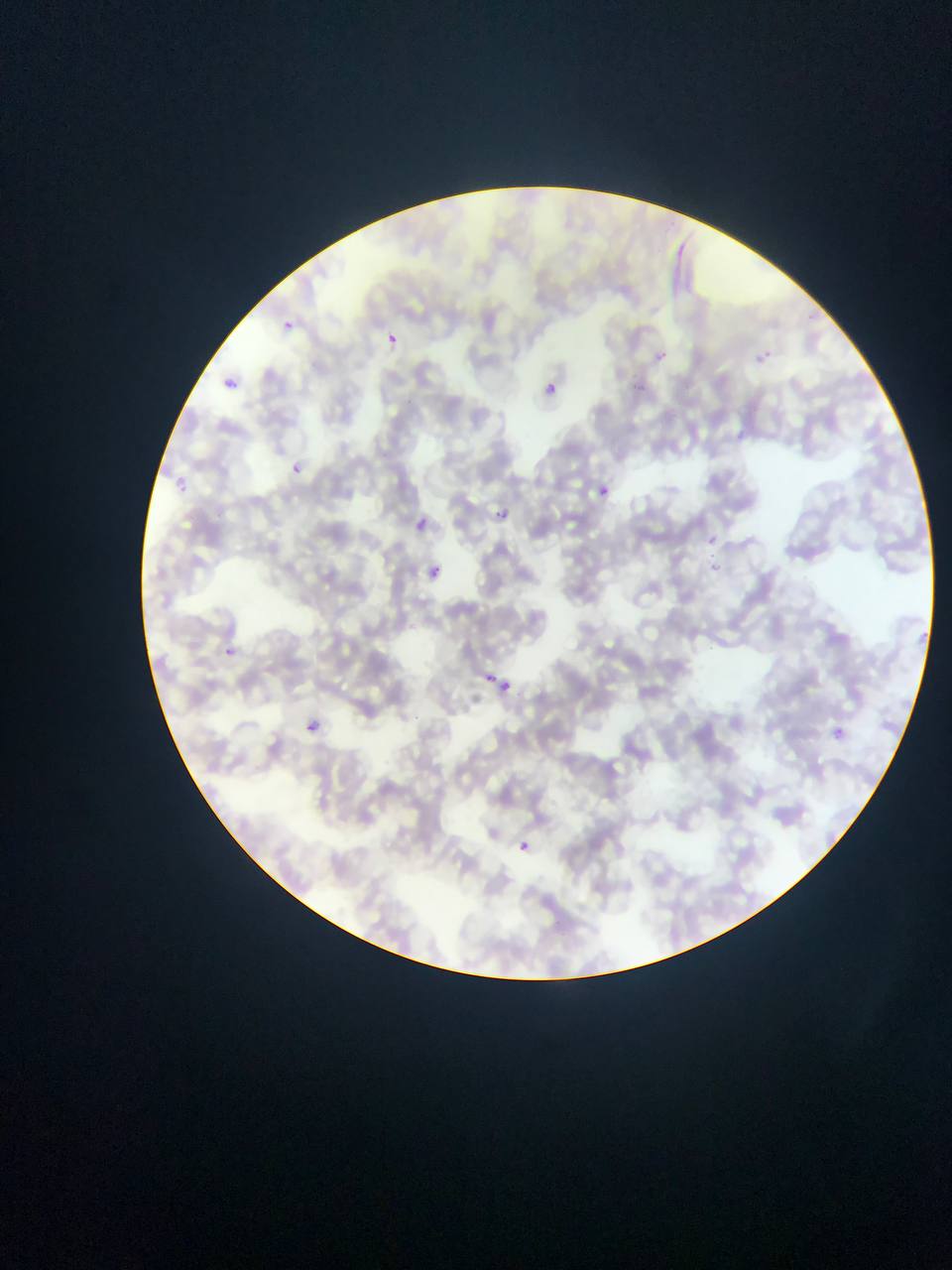

Approximate bounding boxes as left top right bottom in pixels.
Summary:
  - Plasmodium parasite locations: 279 317 297 339; 381 331 397 359; 218 376 232 390; 544 377 572 399; 290 461 307 477; 177 475 195 495; 599 485 610 497; 494 503 517 520; 416 514 436 532; 703 533 719 542; 706 561 727 576; 431 563 443 584; 223 637 240 660; 487 665 512 681; 493 680 523 697; 307 720 321 732; 834 727 846 738; 518 840 530 853
  - Country: Ghana
  - Field of view: single
  - Capture: mobile-phone photograph through a microscope
  - Image size: 952×1270 pixels
  - Preparation: thin blood smear